Point out each Plasmodium parasite.
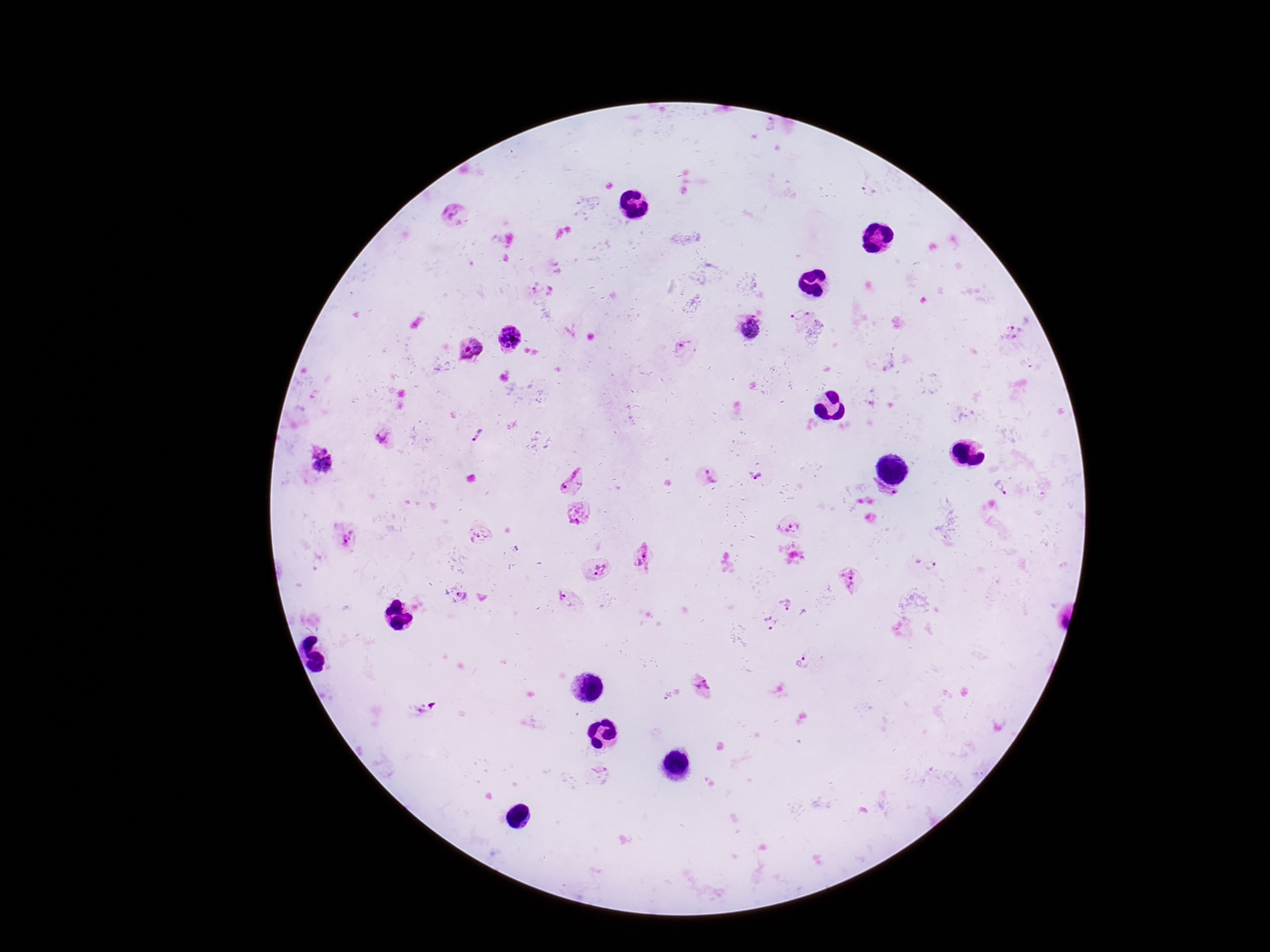

Approximate centers as {x, y} in pixels.
Plasmodium parasites: {772, 125}, {869, 190}, {454, 215}, {537, 292}, {551, 298}, {801, 315}, {750, 328}, {1015, 331}, {509, 337}, {683, 345}, {469, 348}, {478, 435}, {382, 438}, {320, 461}, {709, 475}, {572, 479}, {759, 480}, {1001, 487}, {881, 499}, {576, 510}, {792, 527}, {476, 534}, {346, 538}, {644, 559}, {930, 566}, {600, 569}, {848, 579}, {563, 595}, {460, 596}, {784, 604}, {769, 623}, {803, 664}, {701, 685}, {600, 771}.

Summary:
  - Field of view: one from this slide
  - Magnification: 100x
  - Capture: smartphone camera through the microscope eyepiece
  - Preparation: thick peripheral-blood smear
  - Stain: Giemsa
  - Image size: 1270×952 pixels
  - Patient malaria status: positive